Assess the morphology of the erythrocytes.
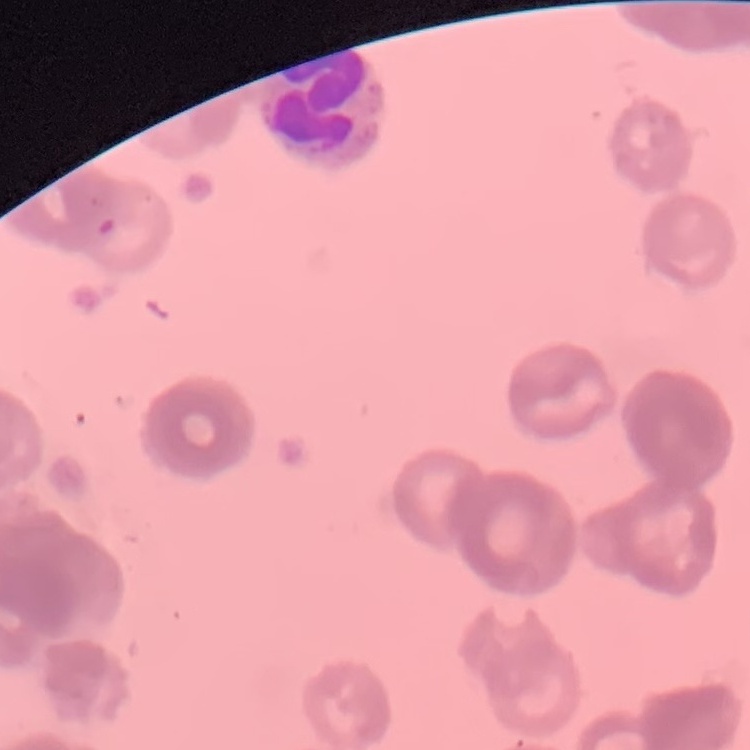
Rouleaux formation.

Thin blood smear. Field's or Giemsa stain. Square crop of a larger photomicrograph.